Report the malaria status of this cell.
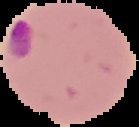

It is parasitized.

The area outside the segmented cell region is set to black. From a thin blood smear. Image is 139×127 pixels.